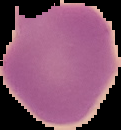
Summary:
  - Malaria status: uninfected
  - Image size: 121×130 pixels
  - Preparation: thin blood smear
  - Image type: segmented cell region with the area outside set to black